Assess this cell for malaria.
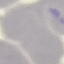
Uninfected.

Photographed with a smartphone camera at the microscope eyepiece. Giemsa-stained preparation. Automatically extracted cell patch, resized to 64 × 64 pixels. Thin smear of blood.